Locate and identify every blood parasite.
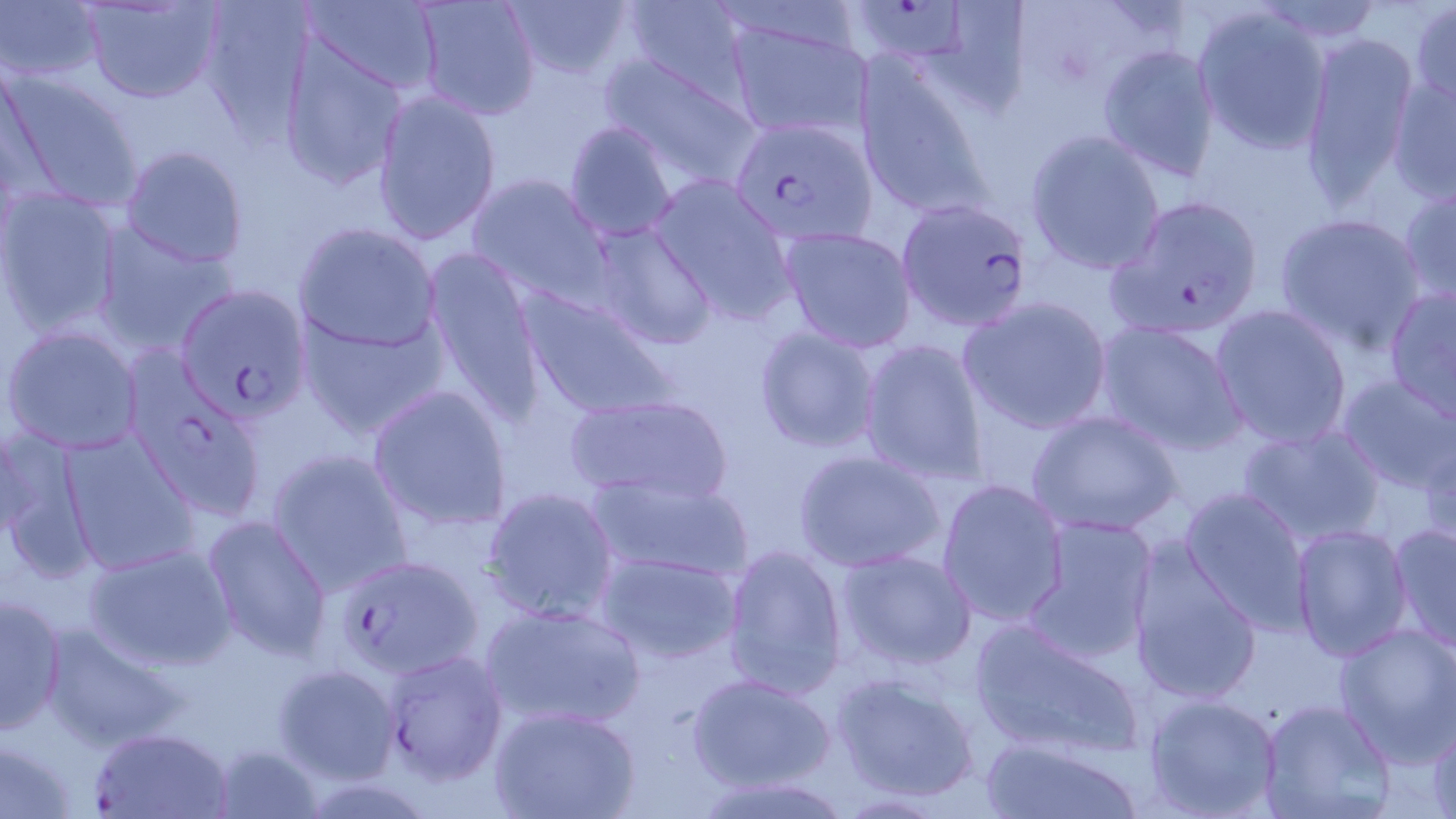
Approximate bounding boxes as (x1,y1)-(x2,y2) corner pairs in pixels.
Plasmodium falciparum-infected red blood cells: (869,1)-(971,59), (733,129)-(882,252), (1108,193)-(1268,340), (895,196)-(1036,333), (174,283)-(312,422), (331,551)-(483,678), (380,647)-(509,786), (88,726)-(235,817).
No Plasmodium ovale, Plasmodium malariae, Plasmodium vivax, Babesia divergens, or Trypanosoma brucei observed.

slide_level_diagnosis: Plasmodium falciparum
uninfected_red_blood_cell_locations: 'approximate bounding boxes as (x1,y1)-(x2,y2) corner pairs in pixels: (78,0)-(227,105), (194,0)-(321,140), (301,0)-(443,93), (411,0)-(541,122), (501,0)-(639,83), (927,0)-(1031,116), (0,1)-(105,84), (616,1)-(758,99), (709,1)-(866,56), (1255,1)-(1386,47), (1409,3)-(1456,111), (1192,4)-(1334,157), (722,15)-(877,141), (1298,30)-(1423,211), (278,41)-(408,191), (1097,43)-(1221,182), (596,50)-(763,191), (851,61)-(995,217), (0,63)-(147,214), (1386,70)-(1455,205), (370,89)-(503,245), (563,119)-(679,241), (1025,129)-(1168,275), (118,143)-(249,270), (466,171)-(612,305), (647,172)-(797,322), (1396,179)-(1455,310), (2,188)-(124,337), (1273,211)-(1430,353), (585,219)-(720,350), (91,221)-(239,358), (293,222)-(441,352), (778,225)-(918,353), (424,249)-(546,422), (1383,283)-(1456,425), (516,285)-(681,422), (957,294)-(1114,436), (1207,304)-(1355,449), (296,312)-(448,438), (1093,317)-(1248,456), (2,322)-(146,456), (753,324)-(884,455), (859,336)-(990,485), (122,358)-(267,522), (1334,372)-(1456,495), (366,383)-(515,532), (558,391)-(736,507), (1026,408)-(1184,538), (1236,415)-(1389,546), (1417,424)-(1455,545), (0,426)-(94,582), (59,430)-(200,576), (264,447)-(413,597), (794,448)-(948,574), (588,471)-(754,584), (936,477)-(1070,629), (479,485)-(620,625), (1178,486)-(1314,632), (200,515)-(333,661), (1019,515)-(1160,663), (1388,521)-(1455,655), (1288,523)-(1414,662), (1124,537)-(1265,707), (83,542)-(239,673), (721,542)-(849,701), (834,548)-(978,673), (592,550)-(746,667), (1,591)-(68,733), (479,600)-(646,733), (969,615)-(1145,761), (39,621)-(189,752), (1332,622)-(1456,764), (271,662)-(402,784), (830,667)-(983,804), (686,671)-(837,794), (1141,692)-(1284,819), (1257,698)-(1396,819), (490,705)-(639,819), (1424,717)-(1456,819), (979,734)-(1144,818), (0,736)-(79,817), (208,740)-(325,819)'
preparation: thin blood film
magnification: 1000x
modality: optical microscopy
stain: May-Grünwald-Giemsa
field_of_view: single
image_size: 1456×819 pixels